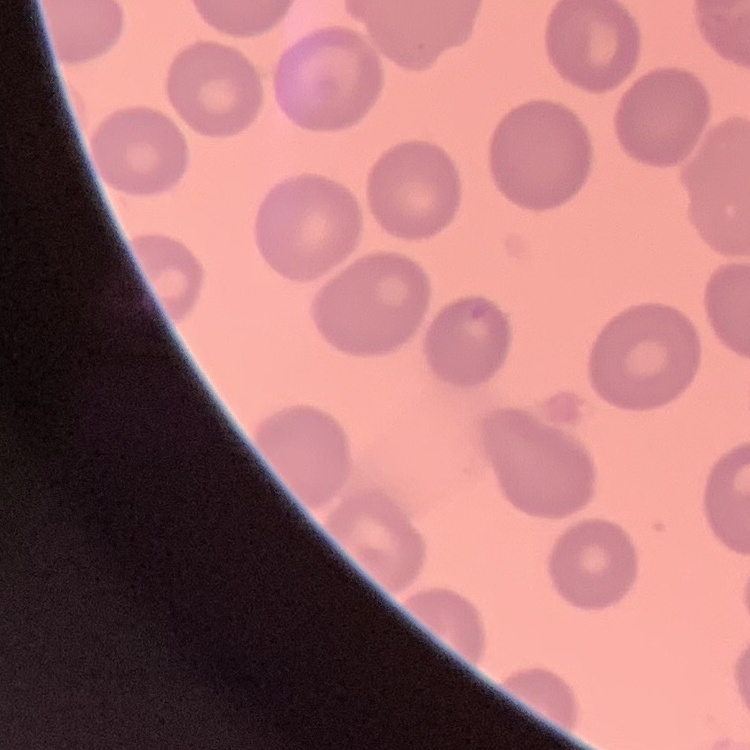 The red blood cells show no rouleaux formation. Thin blood smear. Stained with either Field's or Giemsa. One tile cut from a larger photomicrograph.